Report the malaria status of this cell.
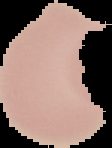

It is uninfected.

Image is 112×148 pixels. Cell region segmented out of the field of view; the surrounding area is masked to black. From a thin blood smear.